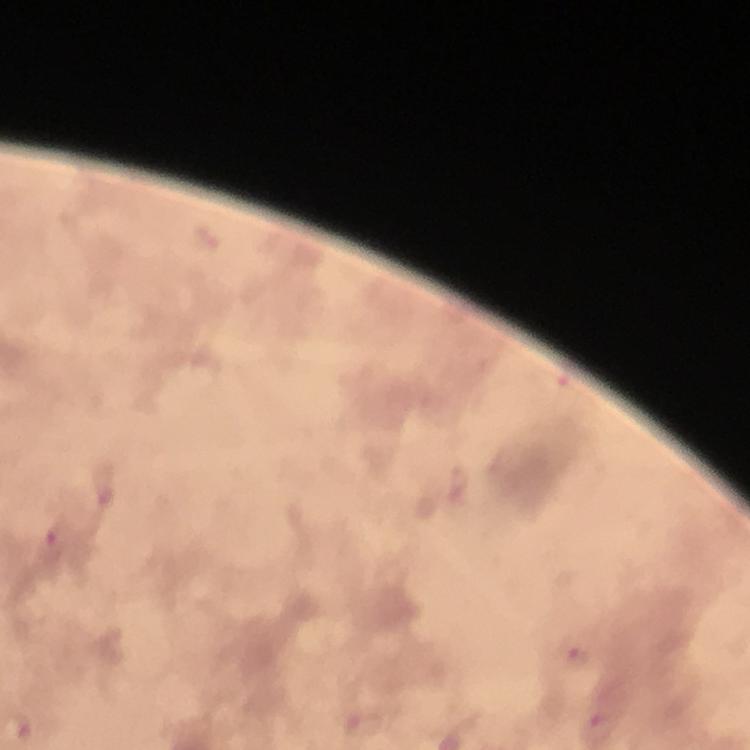
Approximate centers as {x, y} in pixels. Malaria parasite locations: {459, 483}, {105, 485}, {56, 532}, {575, 651}, {598, 728}. Cropped region of a single field of view. Immersion oil was used. From a diagnostic examination for malaria. Image is 750×750 pixels. Giemsa-stained preparation. Thick blood film. Smartphone photograph taken through a microscope. 100x magnification.